Report the malaria status.
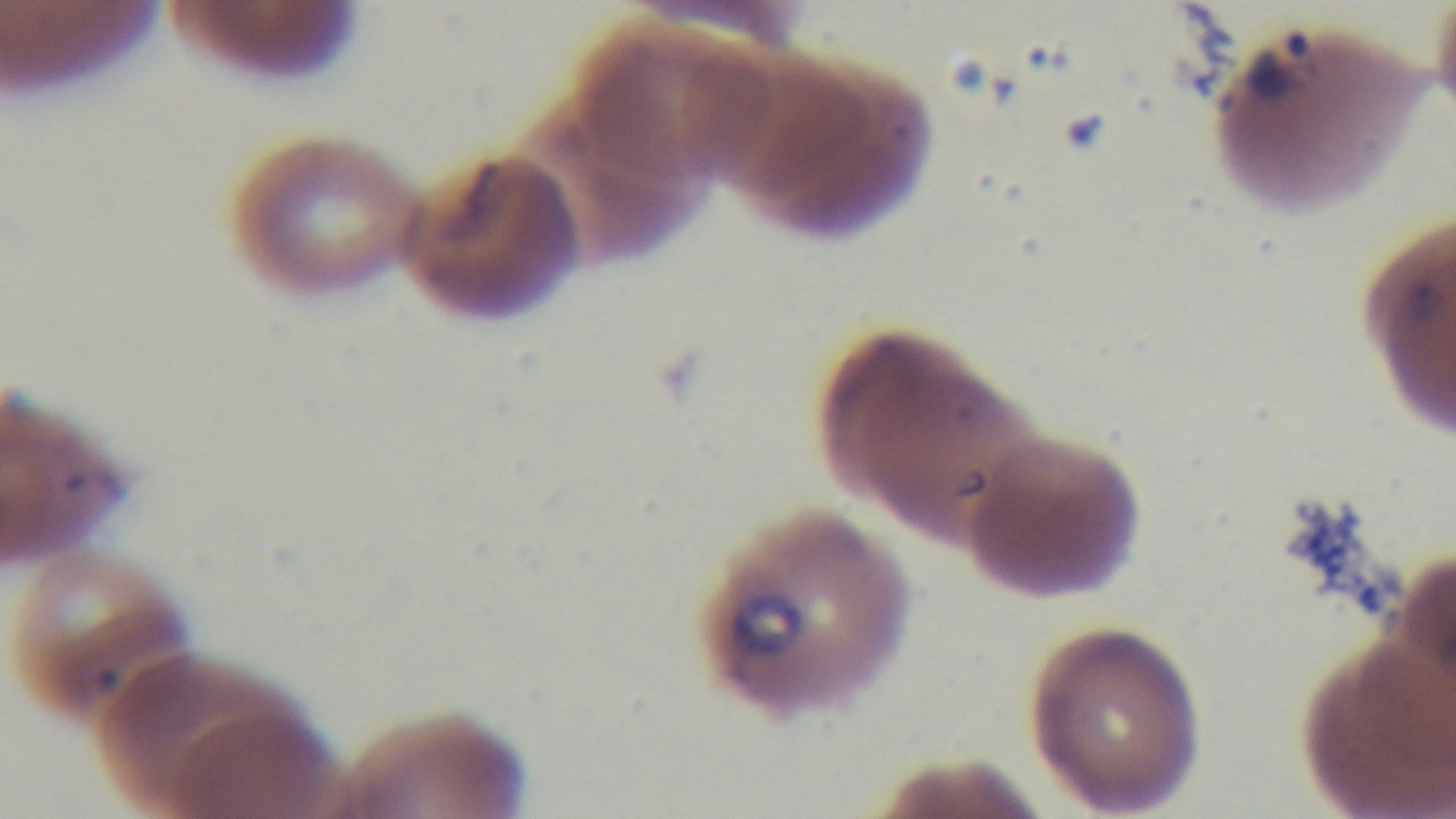
It is infected.

{
  "field_of_view": "one from the slide",
  "objective": "100x oil immersion",
  "stain": "Giemsa",
  "modality": "light microscopy",
  "preparation": "thin smear",
  "capture": "mounted 4K digital camera"
}